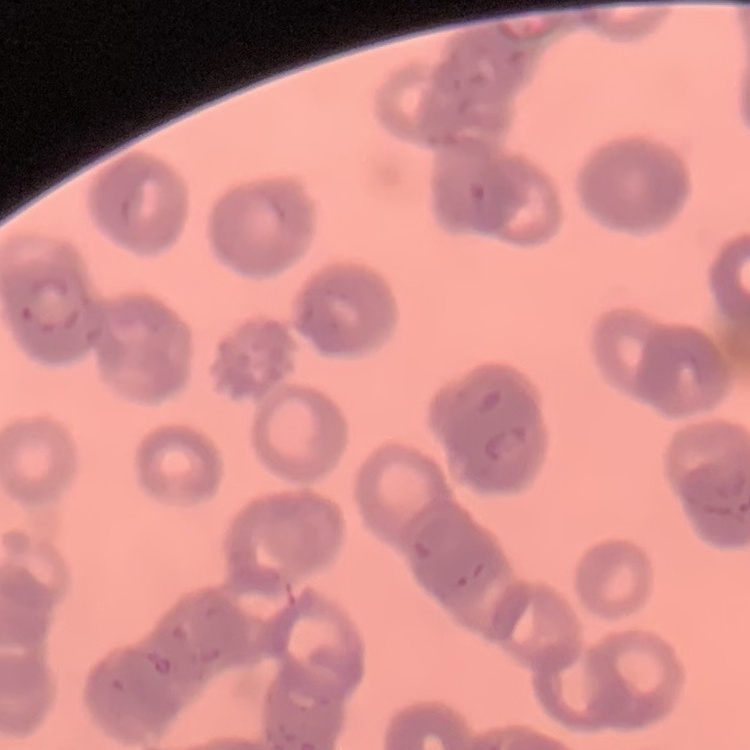
{
  "erythrocyte_morphology": "rouleaux formation",
  "stain": "Field's or Giemsa",
  "image_type": "one tile cut from a larger photomicrograph",
  "preparation": "thin peripheral smear"
}